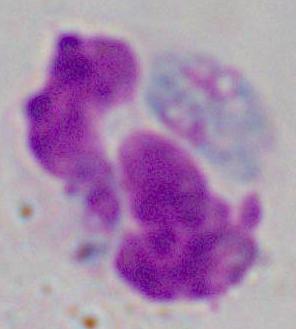

modality: photomicrograph
identification: white blood cell
magnification: 1000x